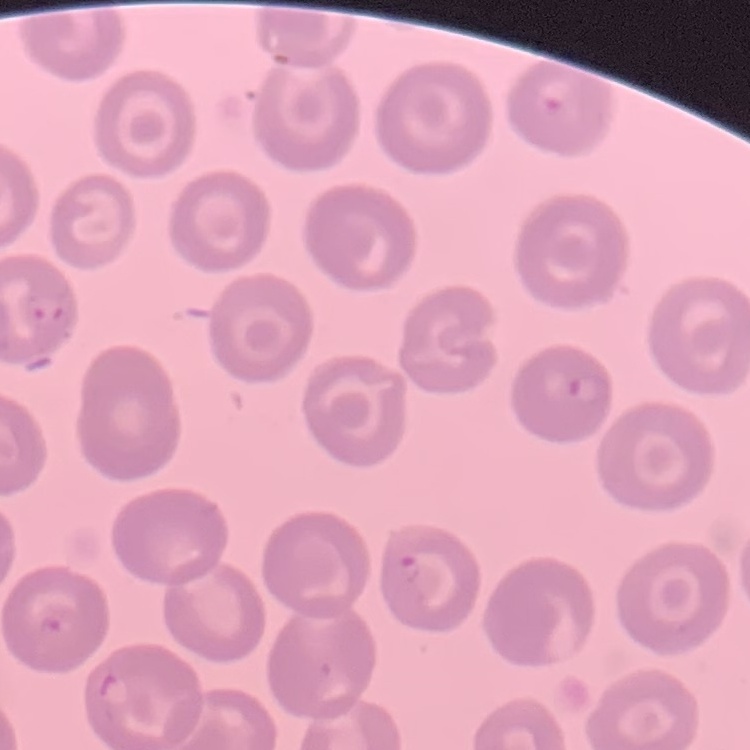 The erythrocytes exhibit no rouleaux formation. Thin blood film. One tile cut from a larger photomicrograph. Stained with either Field's or Giemsa.